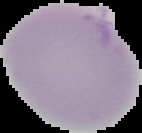

Image is 142×133 pixels. From a thin blood film. Malaria status: uninfected. Cell region segmented out of the field of view; the surrounding area is masked to black.